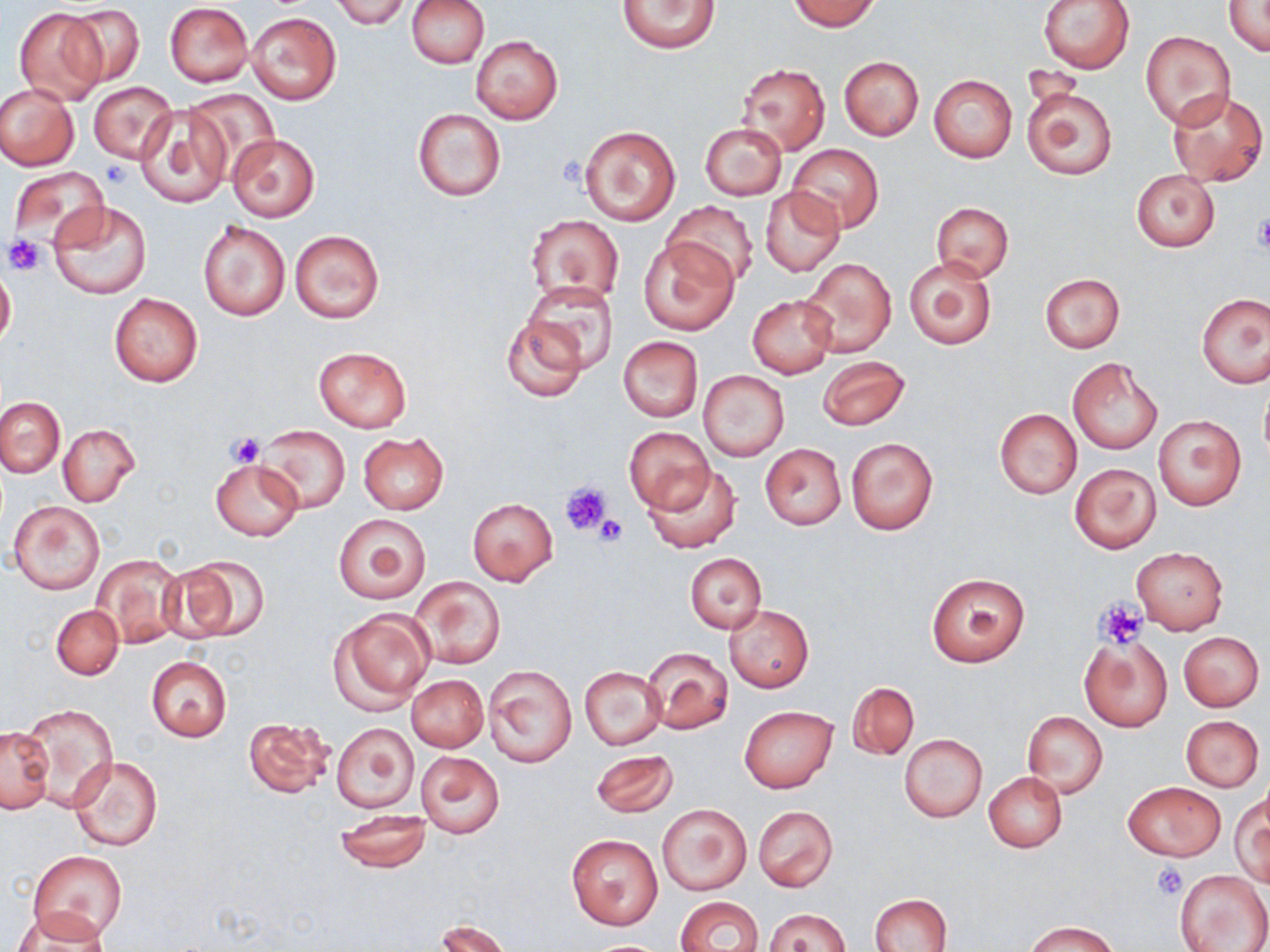 Approximate bounding boxes as (x1,y1)-(x2,y2) corner pairs in pixels. Uninfected red blood cell locations: (331,0)-(410,29), (407,0)-(488,68), (787,0)-(881,31), (1038,0)-(1135,74), (1223,0)-(1270,57), (618,1)-(719,53), (64,3)-(145,88), (164,3)-(253,87), (13,7)-(109,106), (248,12)-(341,104), (1141,31)-(1235,128), (470,35)-(564,125), (838,57)-(923,140), (738,63)-(830,154), (929,74)-(1016,163), (88,82)-(175,164), (1021,83)-(1117,180), (0,85)-(79,169), (1165,89)-(1267,188), (187,90)-(281,179), (134,106)-(233,208), (412,109)-(506,201), (700,122)-(787,199), (578,125)-(681,226), (226,134)-(319,222), (787,145)-(884,234), (9,167)-(109,250), (1132,170)-(1219,252), (760,187)-(844,277), (664,200)-(756,287), (50,201)-(152,299), (930,202)-(1013,281), (525,214)-(625,306), (197,220)-(291,322), (290,229)-(384,323), (638,237)-(739,335), (906,256)-(997,350), (798,257)-(898,358), (0,263)-(16,350), (1038,273)-(1125,353), (523,281)-(619,372), (109,292)-(203,387), (1197,293)-(1269,388), (748,295)-(837,378), (499,313)-(589,404), (618,337)-(703,421), (313,346)-(411,432), (818,356)-(909,431), (1067,357)-(1164,454), (699,370)-(789,461), (1259,385)-(1270,467), (0,396)-(66,476), (994,409)-(1082,498), (1153,415)-(1245,511), (255,423)-(351,514), (58,424)-(139,506), (625,427)-(713,513), (358,432)-(449,514), (846,436)-(939,536), (759,443)-(847,530), (211,459)-(303,540), (1069,462)-(1161,553), (644,466)-(740,552), (467,498)-(557,586), (8,502)-(106,594), (334,513)-(430,603), (1132,547)-(1228,634), (686,553)-(765,633), (163,554)-(268,644), (91,555)-(185,648), (926,572)-(1031,668), (410,576)-(505,670), (51,604)-(123,680), (724,605)-(813,692), (331,609)-(434,711), (1178,632)-(1264,710), (1080,638)-(1172,732), (643,646)-(734,734), (145,656)-(232,742), (482,664)-(576,767), (579,665)-(666,751), (407,674)-(488,752), (847,682)-(919,759), (21,704)-(117,810), (739,706)-(837,793), (1022,712)-(1107,798), (1181,716)-(1264,791), (242,717)-(335,798), (332,723)-(419,812), (1,726)-(55,814), (898,733)-(987,822), (589,750)-(678,818), (416,751)-(504,837), (67,755)-(164,852), (984,773)-(1067,852), (1123,781)-(1225,862), (1231,794)-(1268,887), (658,804)-(750,895), (754,806)-(837,892), (335,811)-(431,871), (566,833)-(663,930), (28,850)-(126,940), (1176,869)-(1269,952), (871,893)-(952,951), (675,897)-(764,952), (764,908)-(850,952), (13,909)-(110,951), (436,918)-(513,951), (1026,920)-(1118,952). Platelet locations: (101,158)-(131,188), (1253,214)-(1270,255), (5,235)-(47,275), (227,431)-(266,467), (558,479)-(612,536), (594,514)-(628,547), (1096,600)-(1148,650), (1152,861)-(1188,900). Slide-level diagnosis: negative for blood parasites. Image is 1270×952 pixels. Single field of view. Light microscopy. Captured at 1000x magnification. May-Grünwald-Giemsa-stained preparation. Thin blood smear.